Point out each leukocyte.
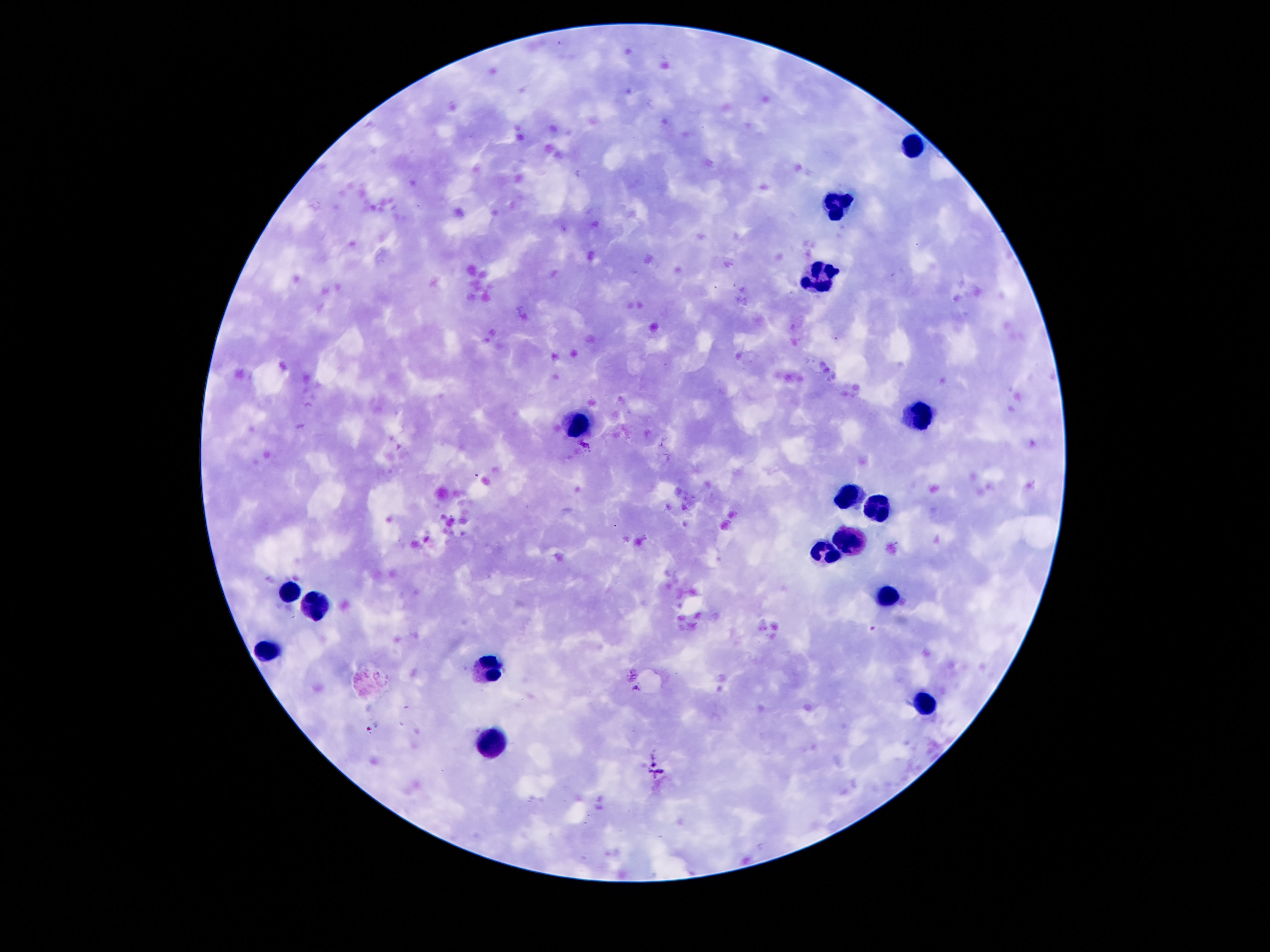

Approximate centers as (x, y) in pixels.
Leukocytes: (913, 146), (838, 208), (819, 273), (913, 414), (576, 426), (845, 496), (877, 506), (845, 537), (821, 551), (288, 590), (884, 599), (315, 606), (269, 650), (490, 669), (925, 707), (487, 743).

100x magnification. Patient malaria status: negative. Single field of view. Giemsa stain. Photographed through the microscope eyepiece with a smartphone camera. Image is 1270×952 pixels. Thick blood smear.